Assess this cell for malaria.
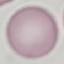

Uninfected.

Thin smear of blood. Cell patch, automatically extracted from a larger field of view and resized to 64 × 64 pixels. Photographed with a smartphone camera at the microscope eyepiece. Giemsa stain.